Outline each blood parasite and name the species.
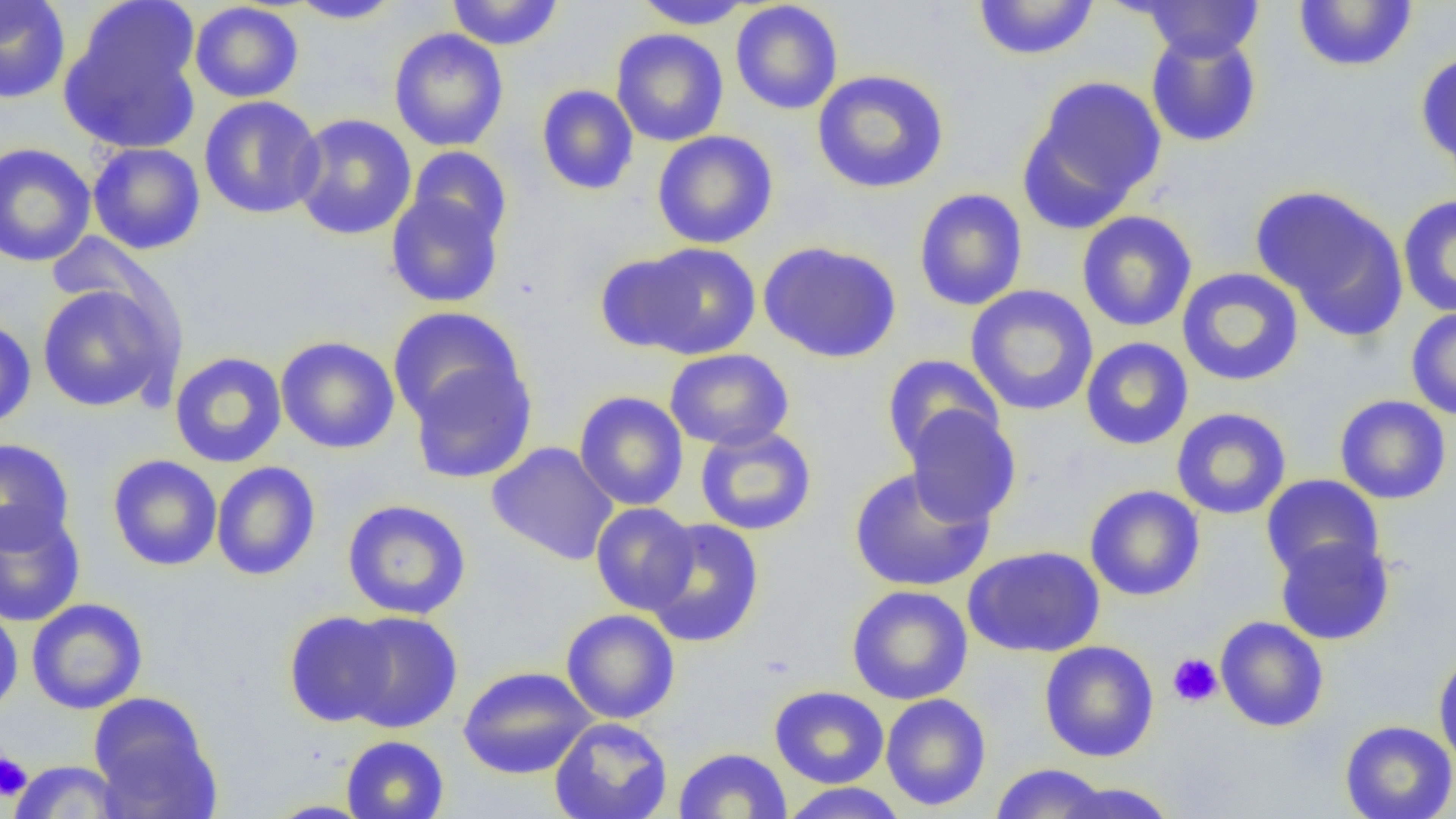

No blood parasites seen.

Summary:
  - Coordinate format: approximate bounding boxes as (x1, y1, x2, y2) in pixels
  - Uninfected red blood cell locations: (0, 0, 71, 105), (288, 0, 403, 24), (446, 0, 564, 51), (633, 0, 754, 30), (1292, 0, 1418, 74), (189, 1, 304, 103), (730, 1, 843, 115), (972, 1, 1100, 61), (1138, 1, 1265, 62), (60, 7, 202, 154), (388, 28, 509, 152), (611, 28, 728, 147), (1145, 30, 1262, 148), (1416, 50, 1456, 175), (812, 69, 949, 194), (1023, 75, 1167, 225), (536, 85, 639, 196), (199, 95, 325, 219), (291, 113, 417, 240), (652, 131, 778, 249), (0, 142, 96, 267), (87, 142, 206, 255), (407, 146, 513, 246), (1252, 185, 1408, 337), (913, 188, 1028, 312), (385, 192, 504, 308), (1397, 195, 1456, 318), (1076, 211, 1198, 332), (758, 240, 902, 363), (631, 242, 761, 359), (594, 250, 704, 353), (1176, 267, 1304, 387), (36, 282, 177, 413), (965, 285, 1098, 416), (387, 307, 525, 428), (1406, 307, 1456, 421), (0, 317, 37, 430), (275, 336, 400, 454), (1080, 337, 1194, 450), (664, 348, 794, 451), (169, 351, 287, 468), (882, 353, 1004, 464), (407, 356, 538, 485), (573, 391, 689, 511), (1334, 395, 1451, 505), (903, 405, 1022, 527), (1171, 407, 1292, 520), (695, 425, 817, 536), (0, 438, 75, 553), (486, 441, 619, 565), (107, 454, 223, 571), (210, 461, 321, 581), (848, 466, 994, 592), (1260, 474, 1384, 583), (1084, 484, 1205, 601), (342, 499, 472, 619), (591, 502, 698, 614), (0, 506, 86, 627), (643, 517, 764, 647), (1274, 534, 1394, 645), (963, 545, 1105, 658), (846, 585, 973, 705), (26, 598, 148, 714), (0, 601, 24, 720), (561, 609, 680, 724), (283, 610, 399, 727), (339, 611, 464, 733), (1215, 615, 1329, 732), (1039, 641, 1159, 762), (1433, 648, 1456, 770), (457, 666, 596, 779), (769, 685, 889, 788), (88, 693, 219, 816), (880, 693, 991, 811), (549, 716, 673, 819), (1339, 720, 1456, 819), (341, 734, 449, 819), (673, 747, 793, 819), (7, 760, 126, 818), (989, 763, 1112, 818), (1053, 781, 1179, 819), (778, 782, 910, 819), (264, 800, 376, 818)
  - Platelet locations: (1167, 653, 1223, 707), (0, 753, 32, 802)
  - Slide-level diagnosis: negative for blood parasites
  - Field of view: one of a larger specimen
  - Image size: 1456×819 pixels
  - Magnification: 1000x
  - Modality: light microscopy
  - Preparation: thin blood film